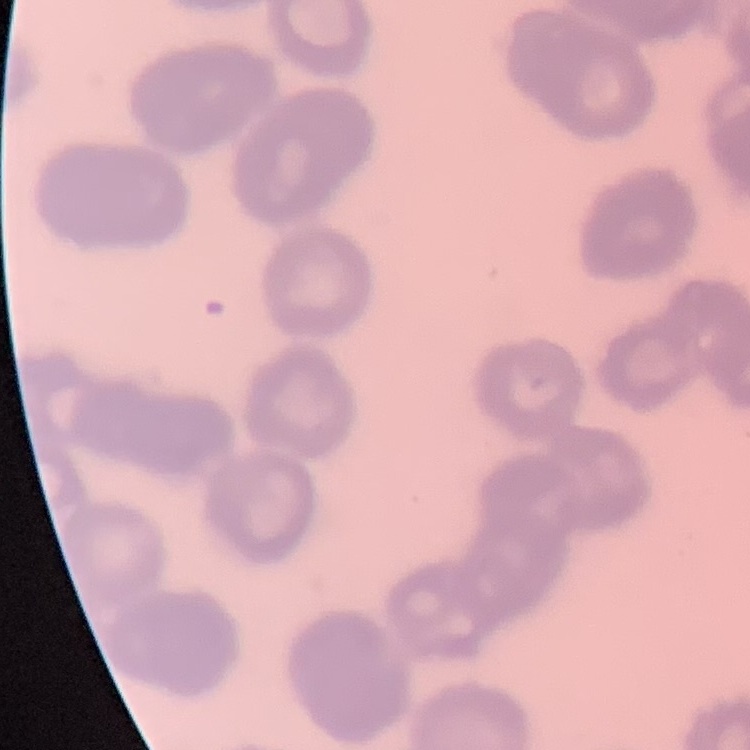

Summary:
  - Red blood cell morphology: rouleaux formation
  - Preparation: thin blood smear
  - Stain: Field's or Giemsa
  - Image type: square crop of a larger photomicrograph